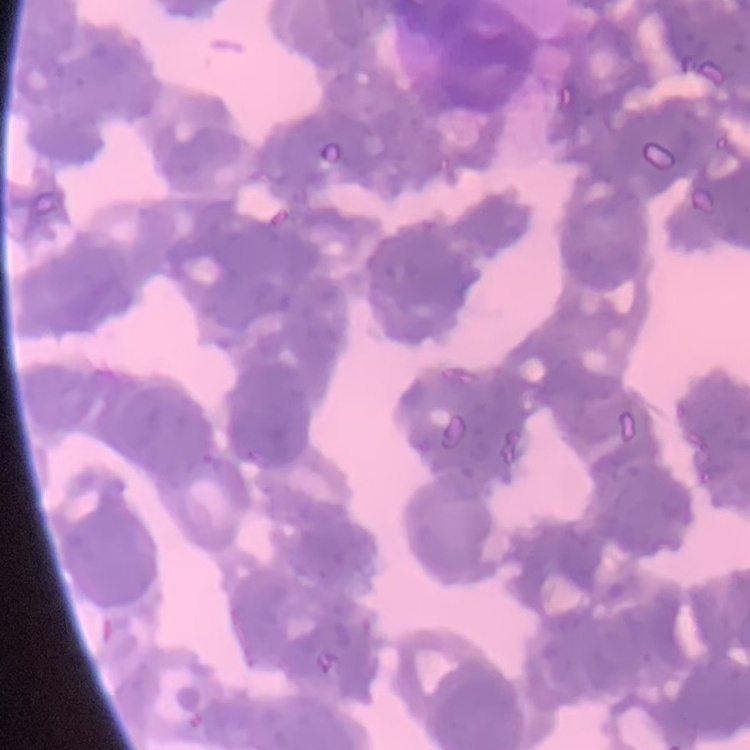
erythrocyte_morphology: rouleaux formation
stain: Field's or Giemsa
preparation: thin blood smear
image_type: square crop of a larger photomicrograph